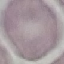

{
  "malaria_status": "uninfected",
  "image_type": "automatically extracted cell patch, resized to 64 × 64 pixels",
  "preparation": "thin blood smear",
  "stain": "Giemsa",
  "capture": "smartphone through the microscope eyepiece"
}